Name the cell type shown.
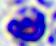

This is a leukocyte.

{
  "modality": "photomicrograph",
  "magnification": "400x"
}